Point out each Plasmodium parasite.
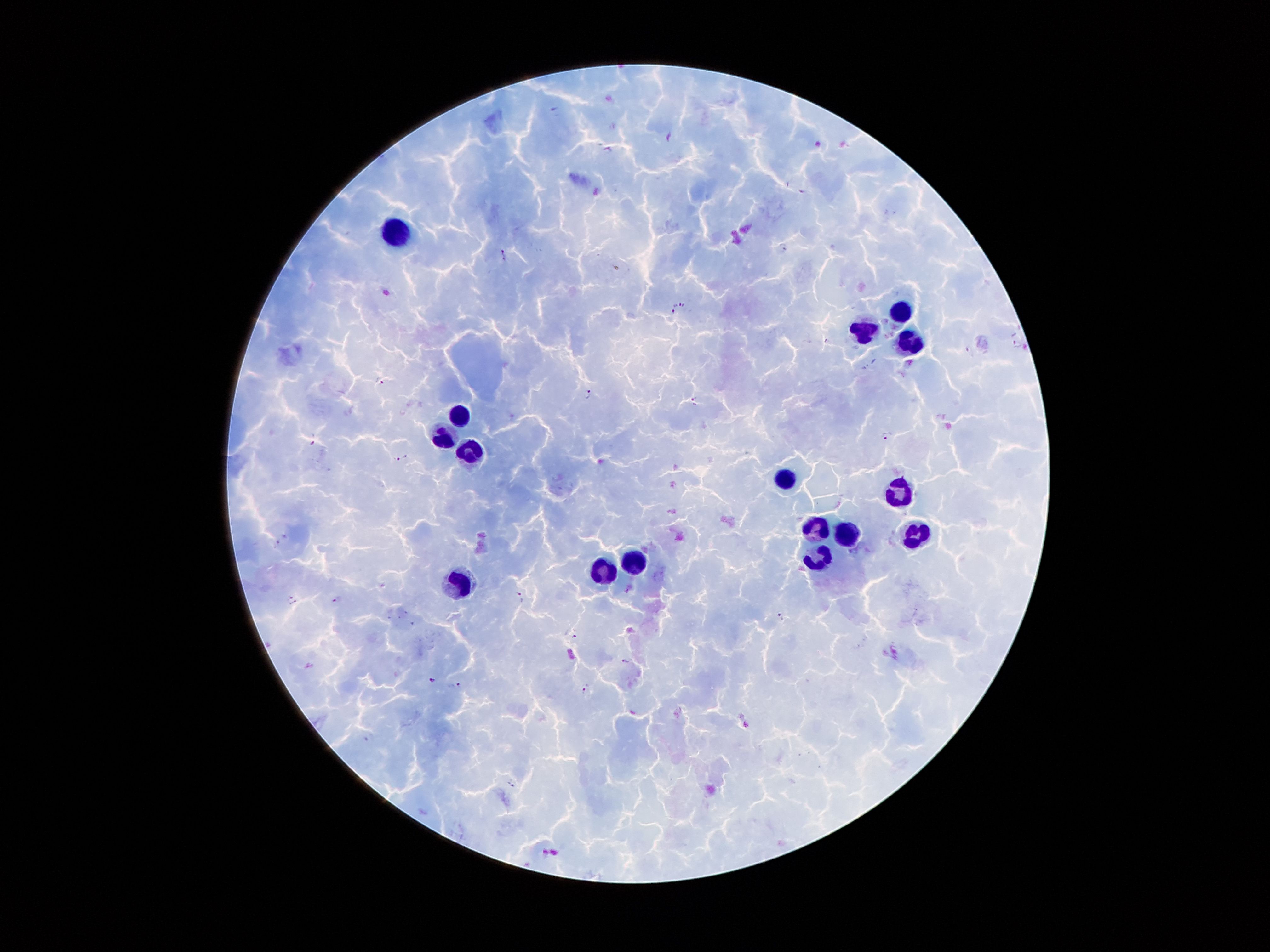
Approximate object centers, in pixels from the top-left corner.
Plasmodium parasites: (x=803, y=192), (x=783, y=245), (x=505, y=254), (x=679, y=304), (x=674, y=310), (x=1017, y=344), (x=381, y=380), (x=587, y=394), (x=695, y=400), (x=886, y=435), (x=313, y=442), (x=399, y=459), (x=277, y=544), (x=521, y=596), (x=290, y=597), (x=338, y=599), (x=294, y=602), (x=406, y=612), (x=780, y=616), (x=388, y=617), (x=398, y=617), (x=413, y=623), (x=574, y=636), (x=624, y=661), (x=433, y=679), (x=458, y=683), (x=586, y=688), (x=369, y=737), (x=512, y=784).

leukocyte locations = (x=394, y=232), (x=903, y=309), (x=866, y=331), (x=910, y=339), (x=464, y=413), (x=446, y=438), (x=470, y=453), (x=783, y=475), (x=900, y=491), (x=816, y=525), (x=846, y=531), (x=918, y=532), (x=817, y=558), (x=635, y=563), (x=605, y=573), (x=458, y=582)
preparation = thick blood film
field of view = single
image size = 1270×952 pixels
capture = smartphone through the microscope eyepiece
patient malaria status = infected with Plasmodium falciparum
magnification = 100x
stain = Giemsa